Point out each leukocyte.
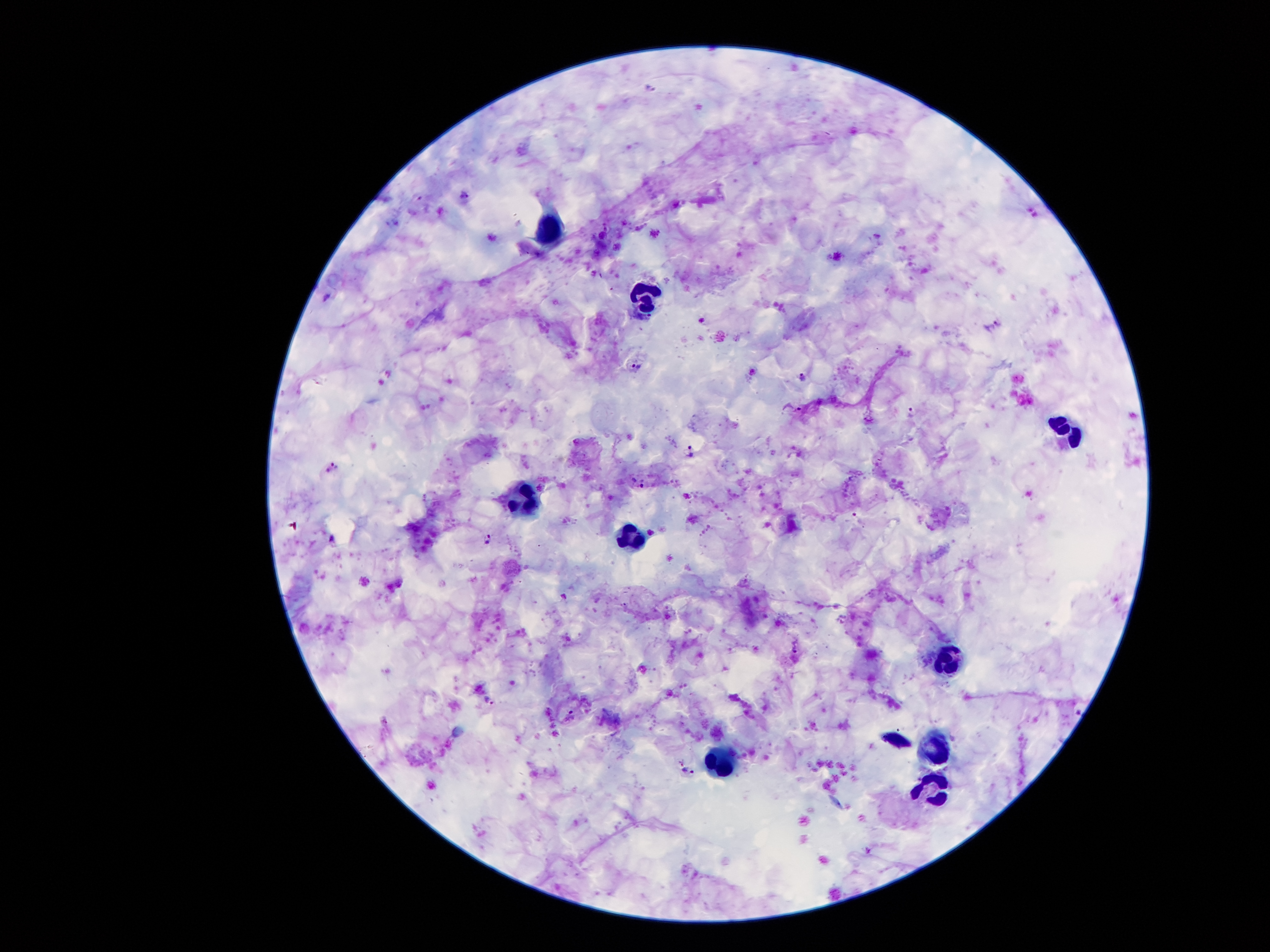

Approximate centers as (x, y) in pixels.
Leukocytes: (547, 232), (644, 297), (1070, 432), (528, 503), (628, 542), (947, 656), (935, 746), (725, 756), (935, 787).

Plasmodium parasite locations = (652, 89), (465, 195), (994, 327), (638, 368), (805, 378), (793, 408), (912, 412), (691, 452), (333, 467), (638, 482), (858, 518), (488, 539), (795, 646), (490, 701), (571, 715), (681, 762), (689, 772)
image size = 1270×952 pixels
field of view = one from this slide
capture = smartphone camera through the microscope eyepiece
magnification = 100x
patient malaria status = positive for Plasmodium falciparum
preparation = thick blood smear
stain = Giemsa